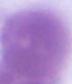

Captured at 1000x magnification. A red blood cell is shown. Micrograph.